Identify the parasite.
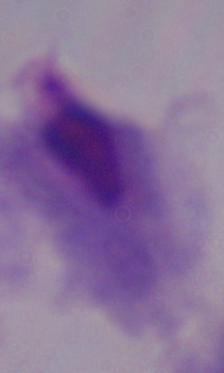

A trichomonad.

{
  "magnification": "1000x",
  "modality": "micrograph"
}